Classify this cell by malaria status.
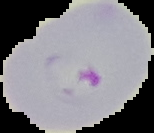
Parasitized.

Summary:
  - Image type: segmented cell region on a black background
  - Image size: 154×133 pixels
  - Preparation: thin blood film